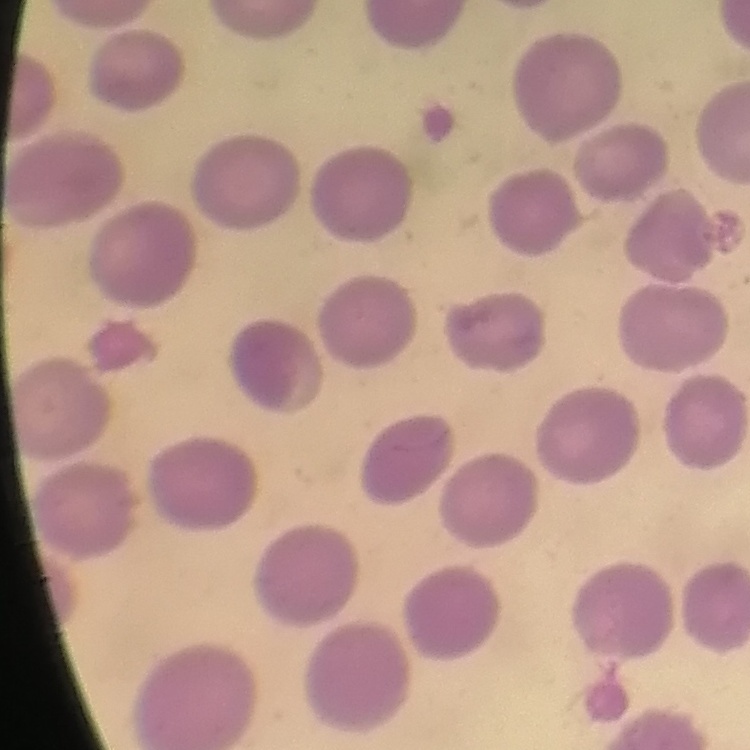
red blood cell morphology = no rouleaux formation
stain = Field's or Giemsa
preparation = thin peripheral smear
image type = one tile cut from a larger photomicrograph